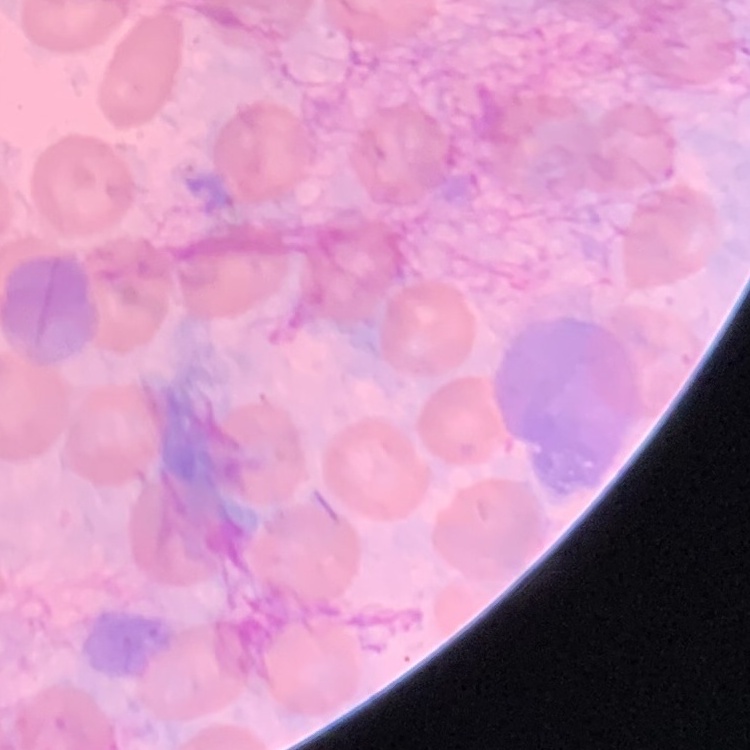 The erythrocytes exhibit no rouleaux formation. Square crop of a larger photomicrograph. Field's or Giemsa stain. Thin blood film.